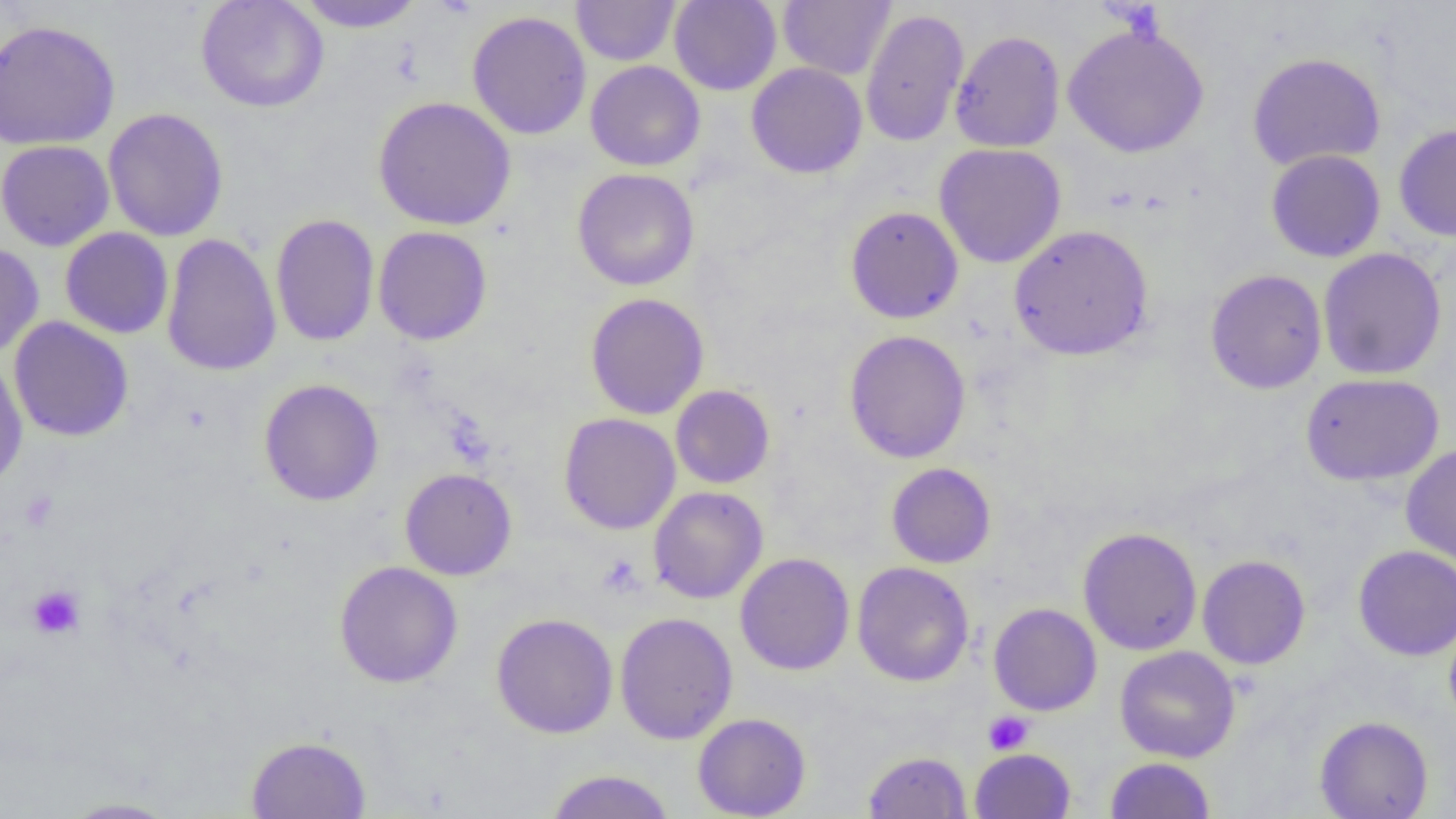

{
  "slide_level_diagnosis": "negative for blood parasites",
  "preparation": "thin blood film",
  "magnification": "1000x",
  "field_of_view": "single",
  "uninfected_red_blood_cell_locations": "approximate bounding boxes as (x1,y1)-(x2,y2) corner pairs in pixels: (196,0)-(329,112), (293,0)-(427,33), (571,0)-(679,66), (669,0)-(781,96), (778,0)-(896,80), (860,8)-(969,148), (466,10)-(592,140), (0,19)-(120,150), (1062,22)-(1209,158), (950,29)-(1066,153), (1247,51)-(1386,171), (585,60)-(705,171), (746,62)-(867,179), (373,96)-(516,231), (102,107)-(229,242), (1394,122)-(1456,241), (0,139)-(115,251), (934,143)-(1066,268), (1266,149)-(1386,262), (572,167)-(700,290), (845,205)-(964,324), (270,213)-(380,347), (1009,225)-(1153,361), (373,226)-(492,345), (60,227)-(174,339), (160,232)-(282,376), (0,242)-(44,359), (1317,248)-(1447,380), (1205,269)-(1327,394), (585,292)-(709,419), (8,316)-(134,442), (843,329)-(971,463), (0,357)-(28,490), (1300,372)-(1444,486), (259,379)-(384,506), (671,384)-(775,489), (559,412)-(681,535), (1400,444)-(1456,568), (886,462)-(996,568), (400,467)-(517,580), (648,486)-(768,604), (1077,526)-(1202,655), (1353,544)-(1456,661), (735,552)-(854,675), (1197,554)-(1310,669), (334,561)-(463,688), (852,561)-(974,686), (988,603)-(1102,716), (491,612)-(618,738), (614,612)-(738,745), (1443,617)-(1456,731), (1115,646)-(1240,763), (692,712)-(811,818), (1314,715)-(1433,818), (246,735)-(372,818), (969,748)-(1076,819), (862,750)-(972,818), (1106,757)-(1216,819), (543,769)-(676,818), (57,797)-(183,818)",
  "image_size": "1456×819 pixels",
  "modality": "optical microscopy",
  "platelet_locations": "approximate bounding boxes as (x1,y1)-(x2,y2) corner pairs in pixels: (18,490)-(60,532), (27,584)-(85,640), (983,711)-(1034,755)"
}